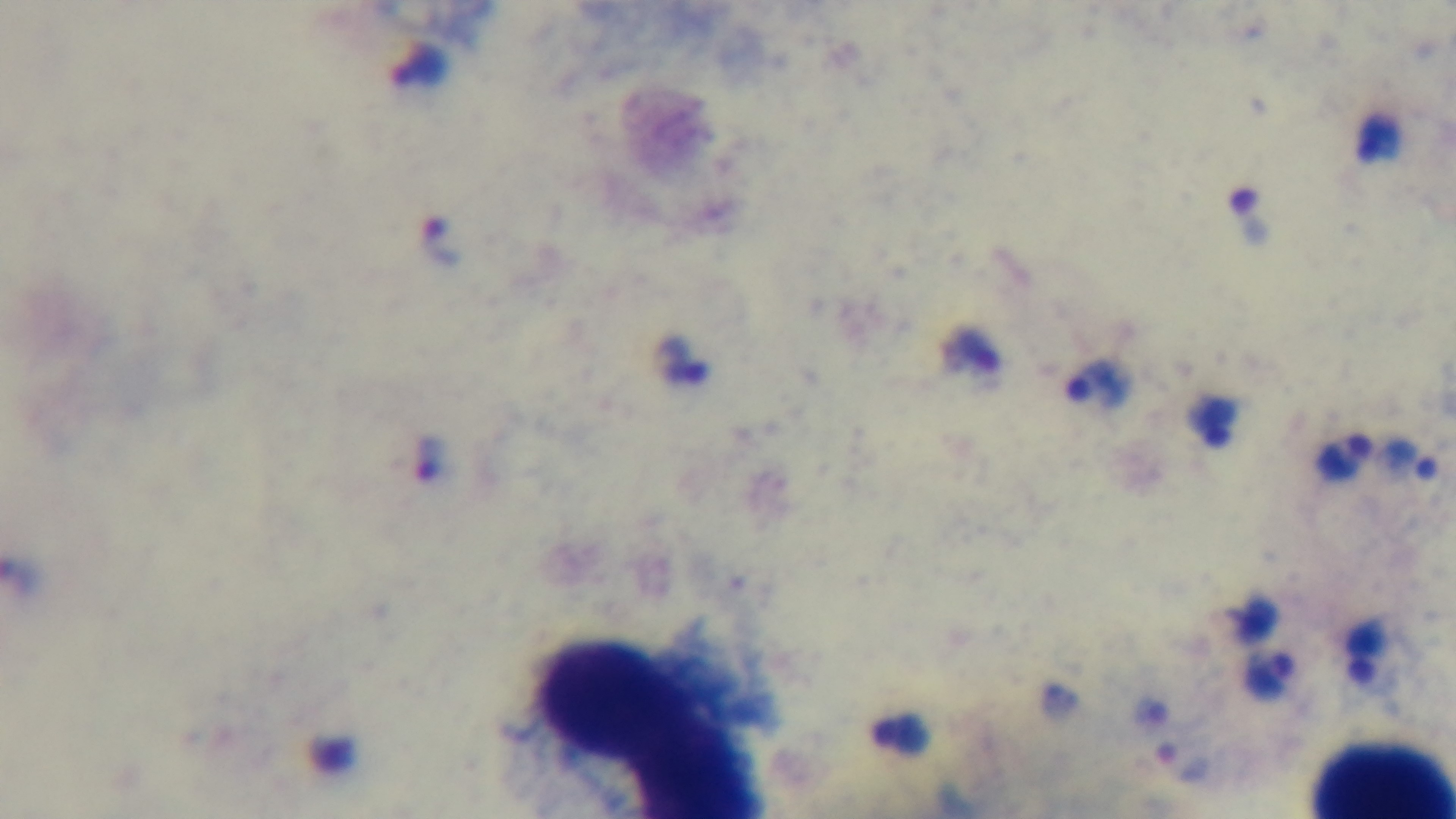

field_of_view: one from the slide
capture: mounted 4K digital camera
stain: Giemsa
preparation: thick blood film
modality: light microscopy
malaria_status: positive
objective: 100x oil immersion